Report the malaria status of this cell.
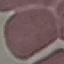

Uninfected.

Summary:
  - Stain: Giemsa
  - Image type: automatically extracted cell patch, resized to 64 × 64 pixels
  - Capture: smartphone camera at the microscope eyepiece
  - Preparation: thin blood film